Report the malaria status of this cell.
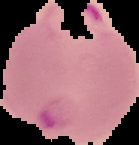

It is parasitized.

Summary:
  - Image type: cell region segmented out of the field of view; surrounding area masked to black
  - Image size: 139×145 pixels
  - Preparation: thin blood film